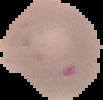

image_size: 103×100 pixels
malaria_status: uninfected
image_type: cell region segmented out of the field of view; surrounding area masked to black
preparation: thin blood film